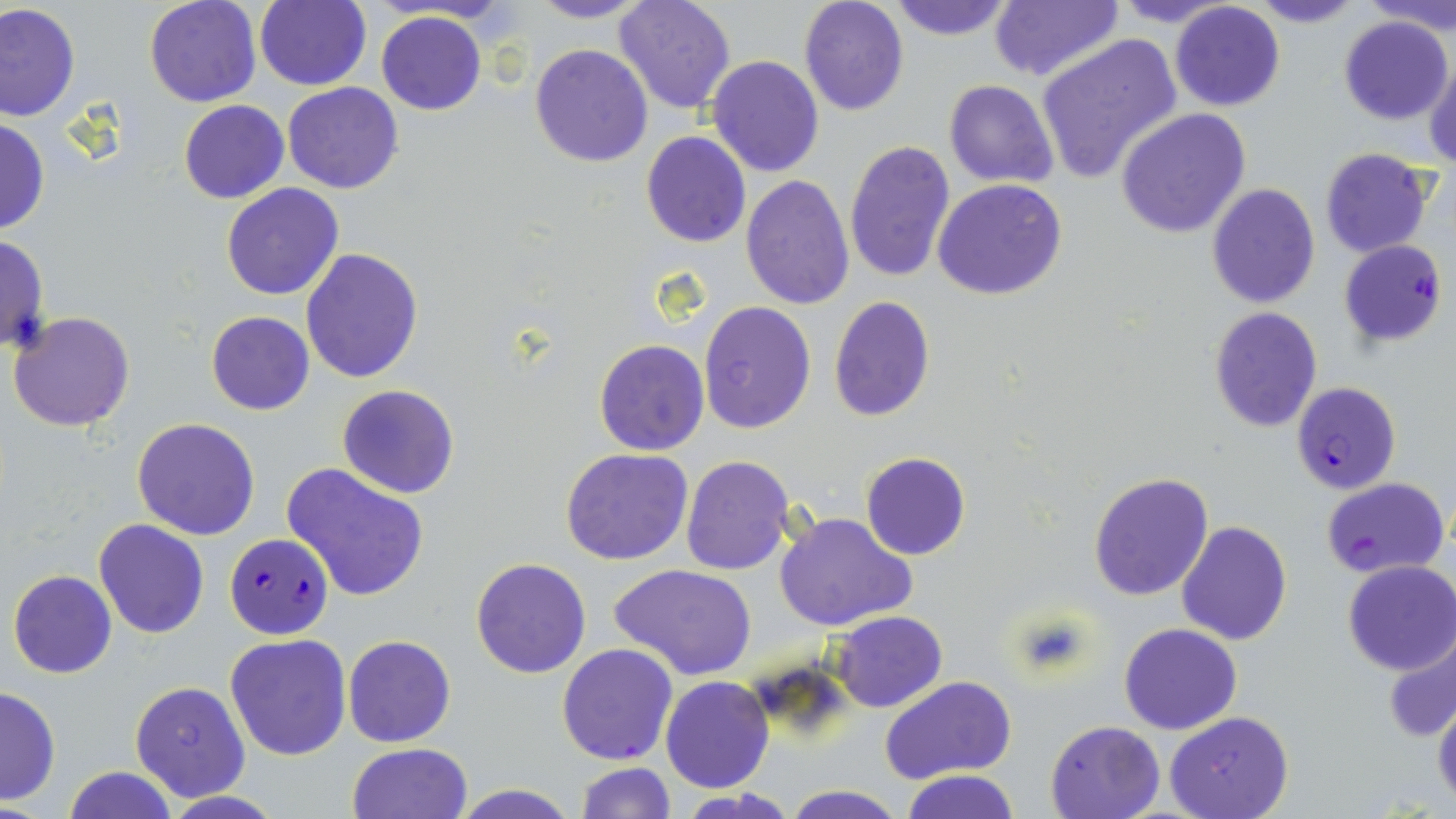

Approximate bounding boxes as named x1/y1/x2/y2 corners in pixels. Plasmodium falciparum-infected red blood cell locations: (x1=1339, y1=239, x2=1448, y2=348), (x1=1291, y1=382, x2=1400, y2=495), (x1=1322, y1=477, x2=1450, y2=581), (x1=225, y1=533, x2=331, y2=639), (x1=556, y1=643, x2=679, y2=766). Uninfected red blood cell locations: (x1=144, y1=0, x2=263, y2=108), (x1=528, y1=0, x2=654, y2=23), (x1=613, y1=0, x2=738, y2=114), (x1=798, y1=0, x2=910, y2=117), (x1=886, y1=0, x2=1017, y2=41), (x1=989, y1=0, x2=1122, y2=83), (x1=1110, y1=0, x2=1242, y2=28), (x1=1244, y1=0, x2=1366, y2=28), (x1=1367, y1=0, x2=1456, y2=34), (x1=254, y1=1, x2=370, y2=90), (x1=1169, y1=2, x2=1285, y2=112), (x1=0, y1=3, x2=81, y2=121), (x1=376, y1=10, x2=487, y2=116), (x1=1339, y1=15, x2=1454, y2=125), (x1=1036, y1=33, x2=1182, y2=185), (x1=529, y1=44, x2=653, y2=167), (x1=706, y1=55, x2=824, y2=177), (x1=1424, y1=58, x2=1456, y2=171), (x1=943, y1=79, x2=1059, y2=188), (x1=281, y1=82, x2=405, y2=194), (x1=177, y1=101, x2=289, y2=203), (x1=1115, y1=108, x2=1252, y2=239), (x1=0, y1=116, x2=48, y2=236), (x1=640, y1=129, x2=752, y2=249), (x1=844, y1=140, x2=957, y2=286), (x1=1319, y1=148, x2=1434, y2=258), (x1=740, y1=175, x2=855, y2=309), (x1=934, y1=178, x2=1068, y2=300), (x1=1205, y1=182, x2=1320, y2=309), (x1=221, y1=183, x2=344, y2=301), (x1=0, y1=232, x2=50, y2=354), (x1=299, y1=245, x2=423, y2=383), (x1=827, y1=297, x2=935, y2=423), (x1=698, y1=301, x2=815, y2=433), (x1=1209, y1=306, x2=1322, y2=432), (x1=8, y1=308, x2=136, y2=430), (x1=206, y1=311, x2=315, y2=415), (x1=592, y1=323, x2=810, y2=446), (x1=580, y1=338, x2=701, y2=563), (x1=594, y1=340, x2=708, y2=456), (x1=336, y1=385, x2=460, y2=498), (x1=131, y1=418, x2=259, y2=539), (x1=561, y1=448, x2=694, y2=565), (x1=860, y1=452, x2=969, y2=560), (x1=681, y1=455, x2=794, y2=574), (x1=281, y1=462, x2=430, y2=602), (x1=1088, y1=470, x2=1215, y2=601), (x1=774, y1=511, x2=917, y2=632), (x1=1175, y1=519, x2=1292, y2=647), (x1=93, y1=520, x2=208, y2=638), (x1=470, y1=557, x2=592, y2=678), (x1=1341, y1=561, x2=1456, y2=676), (x1=609, y1=565, x2=758, y2=680), (x1=8, y1=570, x2=117, y2=678), (x1=829, y1=612, x2=948, y2=711), (x1=1118, y1=622, x2=1243, y2=734), (x1=1382, y1=627, x2=1456, y2=743), (x1=223, y1=632, x2=352, y2=761), (x1=342, y1=634, x2=456, y2=748), (x1=661, y1=676, x2=773, y2=793), (x1=880, y1=676, x2=1017, y2=787), (x1=129, y1=680, x2=251, y2=802), (x1=0, y1=684, x2=61, y2=807), (x1=1432, y1=696, x2=1456, y2=807), (x1=1163, y1=712, x2=1293, y2=819), (x1=1045, y1=719, x2=1167, y2=818), (x1=346, y1=742, x2=473, y2=819), (x1=574, y1=761, x2=675, y2=818), (x1=62, y1=765, x2=179, y2=819), (x1=902, y1=770, x2=1020, y2=819), (x1=449, y1=782, x2=579, y2=818), (x1=782, y1=785, x2=907, y2=819), (x1=674, y1=789, x2=796, y2=819), (x1=155, y1=792, x2=286, y2=819). Slide-level diagnosis: Plasmodium falciparum. May-Grünwald-Giemsa-stained preparation. Captured at 1000x magnification. Single field of view. Image is 1456×819 pixels. Light microscopy. Thin blood smear.